Name the blood parasite species.
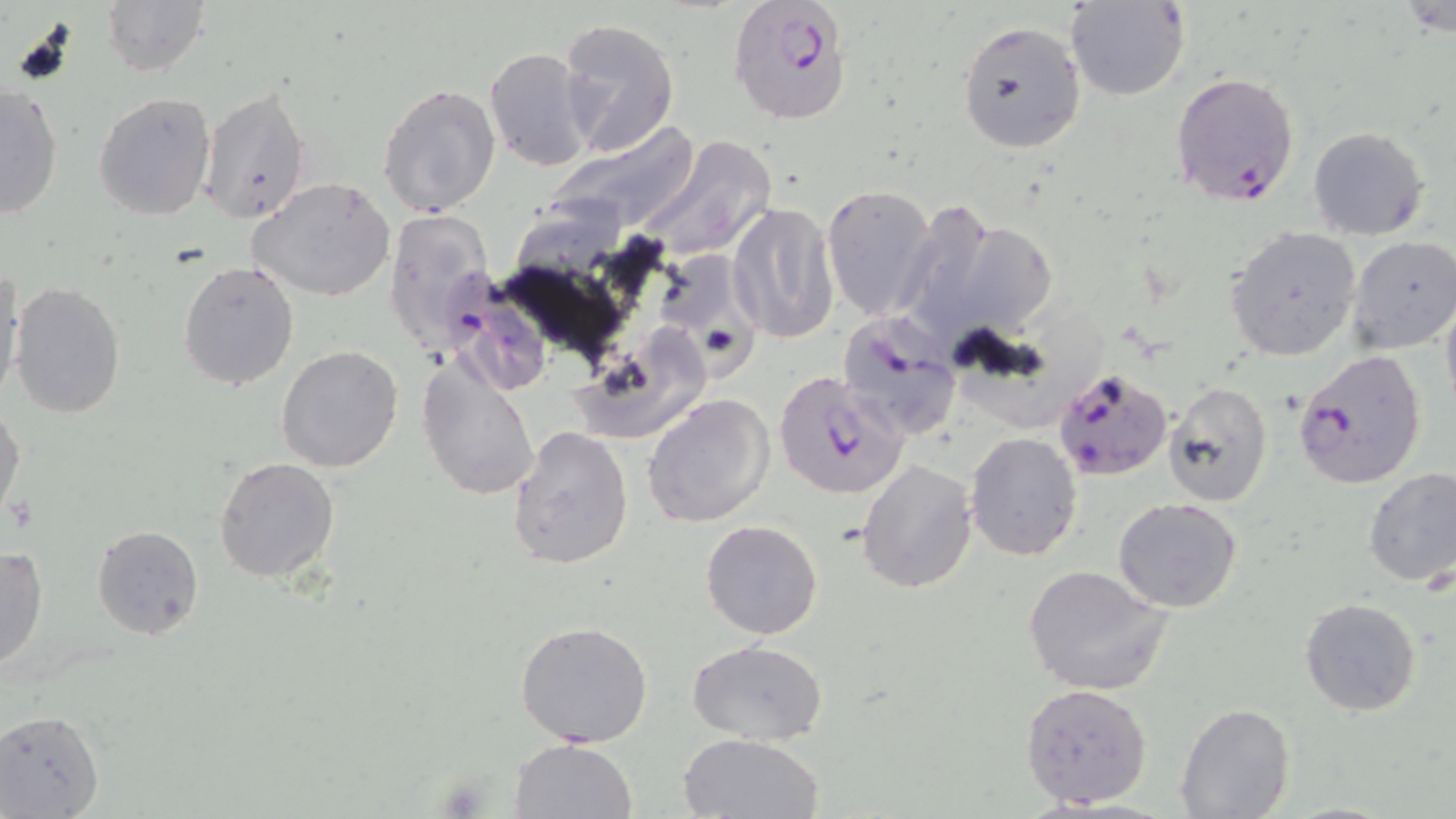

Plasmodium falciparum.

Summary:
  - Coordinate format: approximate bounding boxes as [x1, y1, x2, y2] in pixels
  - Uninfected red blood cell locations: [1066, 0, 1188, 101], [101, 1, 209, 77], [557, 19, 678, 159], [957, 20, 1086, 153], [485, 46, 596, 174], [377, 82, 500, 217], [0, 83, 63, 218], [198, 85, 311, 225], [93, 91, 217, 221], [1308, 127, 1429, 240], [635, 136, 779, 265], [249, 177, 396, 301], [821, 183, 938, 322], [728, 201, 839, 344], [386, 208, 494, 356], [1226, 225, 1363, 362], [1347, 236, 1456, 356], [178, 259, 301, 391], [1, 269, 25, 400], [11, 283, 126, 418], [1441, 293, 1456, 418], [275, 344, 404, 472], [418, 361, 542, 501], [1164, 382, 1273, 504], [644, 392, 774, 527], [0, 404, 23, 521], [507, 426, 634, 570], [966, 432, 1081, 560], [213, 457, 340, 583], [857, 459, 977, 592], [1361, 468, 1456, 589], [1112, 497, 1242, 612], [700, 520, 824, 639], [92, 524, 204, 641], [0, 544, 48, 670], [1023, 563, 1173, 698], [1300, 598, 1421, 716], [515, 620, 653, 747], [686, 639, 828, 745], [1020, 683, 1152, 808], [1174, 702, 1294, 819], [0, 709, 104, 818], [677, 731, 825, 818], [510, 738, 638, 819]
  - Plasmodium falciparum-infected red blood cell locations: [728, 0, 854, 126], [1168, 71, 1300, 208], [448, 265, 551, 397], [836, 312, 962, 441], [1293, 348, 1426, 489], [1053, 367, 1174, 482], [775, 369, 909, 501]
  - Modality: light microscopy
  - Magnification: 1000x
  - Stain: May-Grünwald-Giemsa
  - Field of view: single
  - Preparation: thin blood film
  - Image size: 1456×819 pixels